State which parasite is depicted.
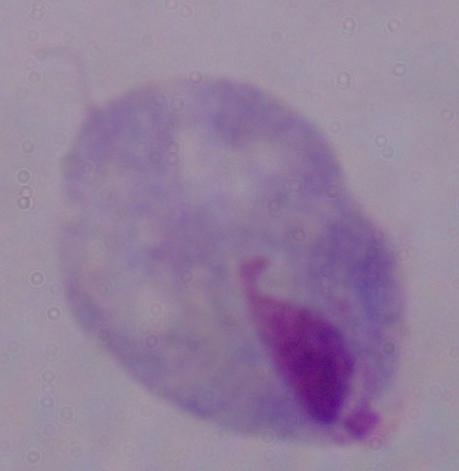
This is a trichomonad.

Summary:
  - Modality: photomicrograph
  - Magnification: 1000x